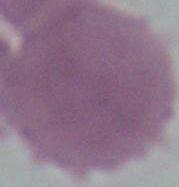
Summary:
  - Identification: red blood cell
  - Magnification: 1000x
  - Modality: photomicrograph